Classify this cell by malaria status.
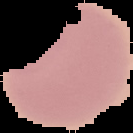
Uninfected.

preparation = thin blood film
image type = cell region segmented out of the field of view; surrounding area masked to black
image size = 133×133 pixels